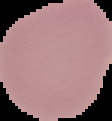
preparation = thin blood smear
image size = 112×121 pixels
image type = segmented cell region on a black background
result = no malaria parasites detected